Locate and identify every blood parasite.
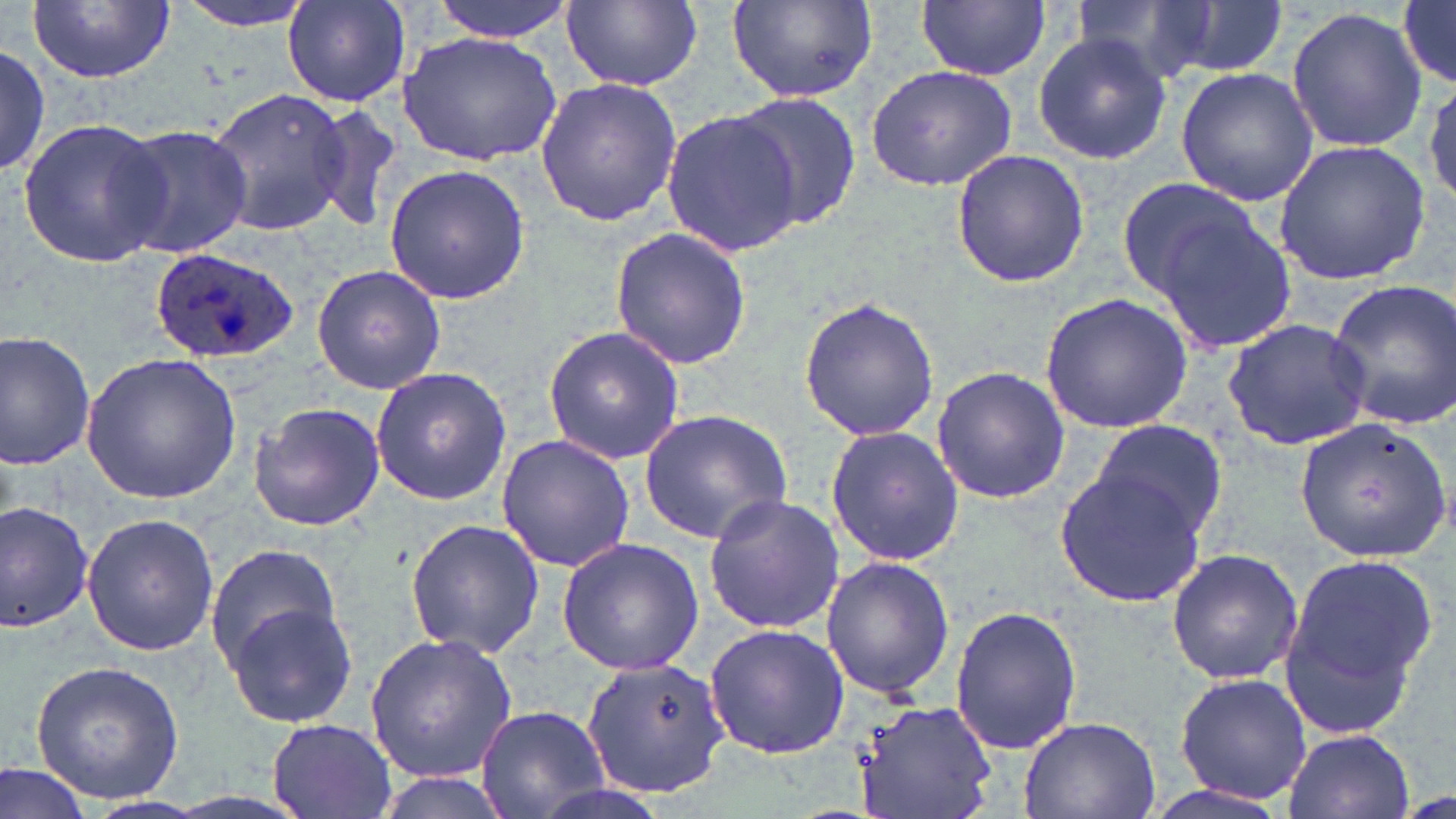
Approximate bounding boxes as named x1/y1/x2/y2 corners in pixels.
Plasmodium ovale-infected red blood cells: (x1=149, y1=248, x2=302, y2=364).
No Plasmodium falciparum, Plasmodium malariae, Plasmodium vivax, Babesia divergens, or Trypanosoma brucei observed.

Uninfected red blood cell locations: (x1=28, y1=0, x2=176, y2=84), (x1=172, y1=0, x2=317, y2=31), (x1=282, y1=0, x2=412, y2=107), (x1=429, y1=0, x2=574, y2=41), (x1=560, y1=0, x2=705, y2=94), (x1=726, y1=0, x2=879, y2=105), (x1=1075, y1=0, x2=1223, y2=83), (x1=918, y1=1, x2=1048, y2=80), (x1=1161, y1=2, x2=1288, y2=76), (x1=1397, y1=3, x2=1456, y2=87), (x1=1285, y1=7, x2=1429, y2=152), (x1=398, y1=30, x2=562, y2=166), (x1=1031, y1=33, x2=1172, y2=165), (x1=0, y1=43, x2=50, y2=176), (x1=865, y1=64, x2=1018, y2=192), (x1=1175, y1=67, x2=1319, y2=206), (x1=1423, y1=71, x2=1456, y2=212), (x1=535, y1=76, x2=681, y2=228), (x1=207, y1=87, x2=348, y2=239), (x1=727, y1=94, x2=865, y2=231), (x1=308, y1=103, x2=404, y2=233), (x1=664, y1=112, x2=802, y2=255), (x1=16, y1=116, x2=168, y2=270), (x1=109, y1=122, x2=253, y2=260), (x1=1273, y1=138, x2=1431, y2=286), (x1=951, y1=151, x2=1090, y2=289), (x1=384, y1=165, x2=529, y2=305), (x1=1115, y1=176, x2=1268, y2=304), (x1=1149, y1=203, x2=1300, y2=355), (x1=610, y1=228, x2=749, y2=370), (x1=311, y1=263, x2=446, y2=394), (x1=1327, y1=279, x2=1456, y2=430), (x1=1039, y1=293, x2=1193, y2=434), (x1=796, y1=294, x2=942, y2=443), (x1=1222, y1=316, x2=1376, y2=451), (x1=542, y1=324, x2=686, y2=465), (x1=0, y1=329, x2=97, y2=473), (x1=80, y1=352, x2=240, y2=504), (x1=371, y1=365, x2=516, y2=505), (x1=931, y1=367, x2=1069, y2=505), (x1=249, y1=402, x2=385, y2=533), (x1=638, y1=409, x2=794, y2=544), (x1=1294, y1=418, x2=1454, y2=561), (x1=1086, y1=419, x2=1231, y2=542), (x1=825, y1=424, x2=964, y2=567), (x1=496, y1=433, x2=633, y2=573), (x1=1054, y1=464, x2=1211, y2=607), (x1=702, y1=494, x2=845, y2=634), (x1=0, y1=500, x2=95, y2=634), (x1=81, y1=512, x2=223, y2=656), (x1=405, y1=519, x2=546, y2=658), (x1=556, y1=537, x2=703, y2=675), (x1=204, y1=542, x2=345, y2=677), (x1=1166, y1=547, x2=1302, y2=686), (x1=1277, y1=548, x2=1440, y2=735), (x1=821, y1=555, x2=955, y2=702), (x1=223, y1=601, x2=363, y2=730), (x1=948, y1=604, x2=1083, y2=757), (x1=702, y1=621, x2=848, y2=760), (x1=365, y1=633, x2=519, y2=782), (x1=581, y1=659, x2=731, y2=799), (x1=30, y1=660, x2=186, y2=804), (x1=1173, y1=673, x2=1315, y2=806), (x1=851, y1=697, x2=998, y2=819), (x1=474, y1=704, x2=608, y2=819), (x1=1017, y1=717, x2=1160, y2=818), (x1=266, y1=718, x2=397, y2=819), (x1=1280, y1=728, x2=1415, y2=819), (x1=0, y1=760, x2=94, y2=819), (x1=1137, y1=778, x2=1298, y2=819). Slide-level diagnosis: Plasmodium ovale. One field of a larger specimen. Captured at 1000x magnification. Light microscopy. Thin blood smear. May-Grünwald-Giemsa-stained preparation. Image is 1456×819 pixels.